Classify this cell by malaria status.
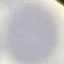
It is uninfected.

capture = smartphone camera at the microscope eyepiece
preparation = thin blood smear
image type = cell patch, automatically extracted from a larger field of view and resized to 64 × 64 pixels
stain = Giemsa